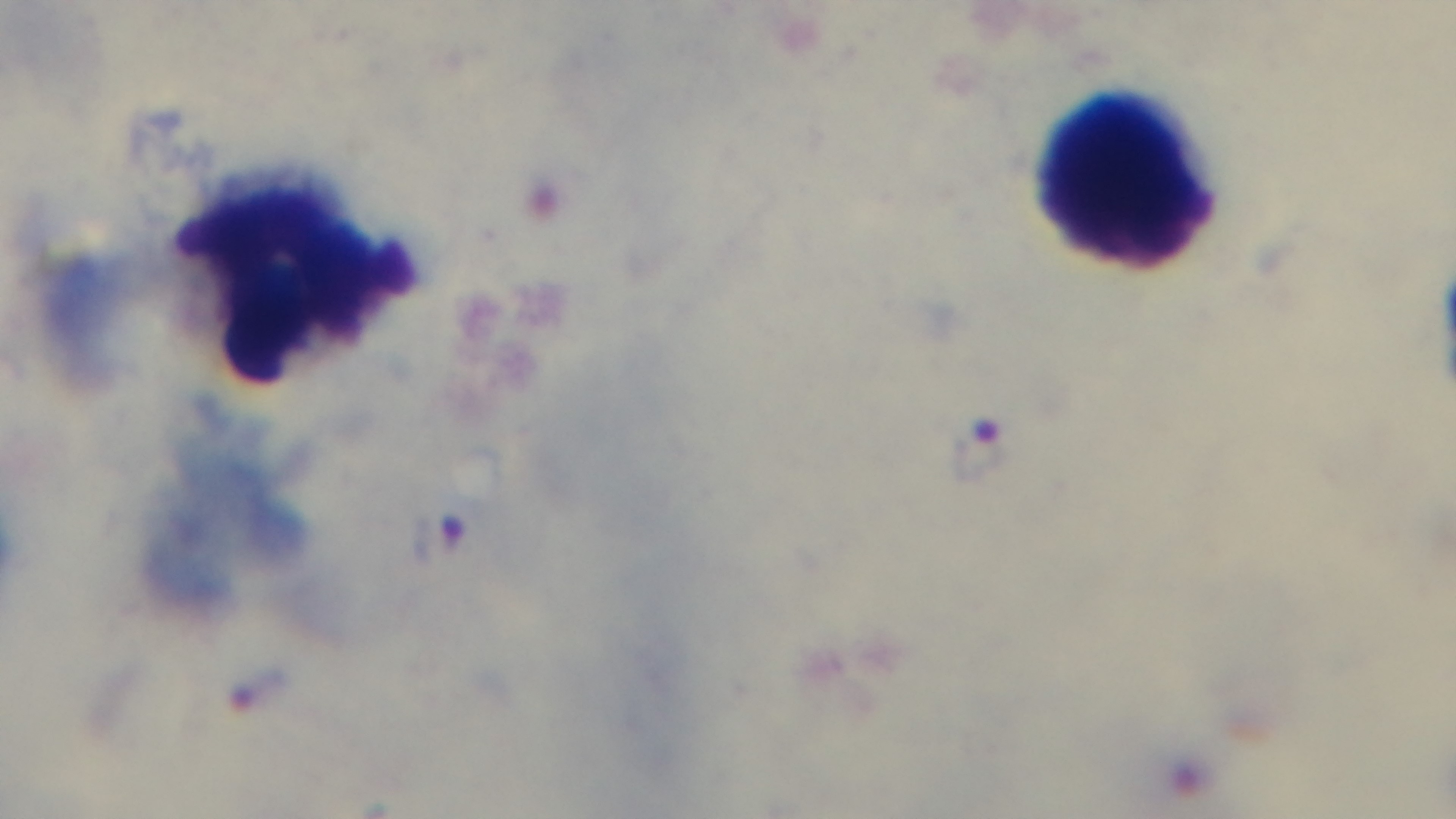

Summary:
  - Capture: mounted 4K digital camera
  - Stain: Giemsa
  - Preparation: thick
  - Field of view: one from the slide
  - Malaria status: infected
  - Modality: light microscopy
  - Objective: 100x oil immersion